Comment on the morphology of the erythrocytes.
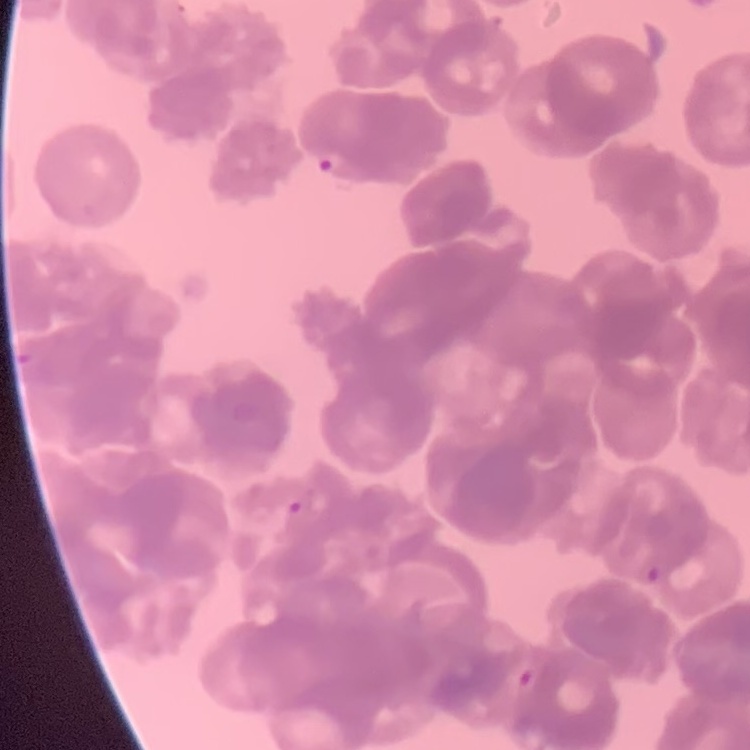

Rouleaux formation.

{
  "preparation": "thin blood smear",
  "stain": "Field's or Giemsa",
  "image_type": "square crop of a larger photomicrograph"
}